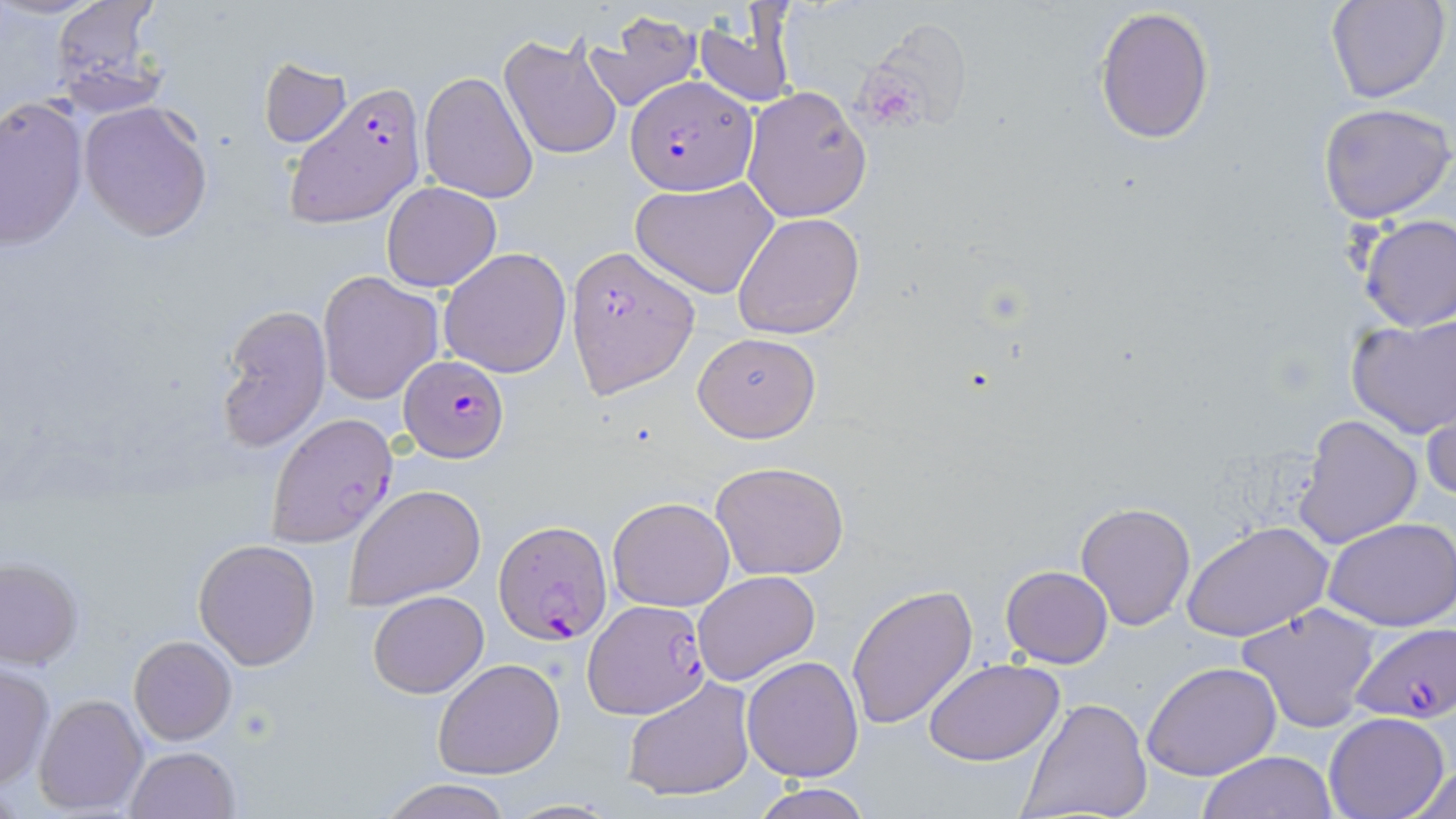
slide-level diagnosis = Plasmodium falciparum
field of view = one of a larger specimen
Plasmodium falciparum-infected red blood cell locations = approximate bounding boxes as (x1, y1, x2, y2) in pixels: (626, 75, 757, 197), (283, 82, 428, 224), (567, 244, 699, 398), (398, 355, 510, 462), (266, 412, 398, 546), (491, 520, 613, 645), (586, 600, 709, 719), (1350, 619, 1456, 726)
image size = 1456×819 pixels
preparation = thin blood film
uninfected red blood cell locations = approximate bounding boxes as (x1, y1, x2, y2) in pixels: (1328, 0, 1450, 103), (49, 1, 167, 108), (1094, 6, 1215, 144), (691, 10, 797, 111), (584, 11, 703, 113), (498, 30, 625, 162), (259, 56, 352, 149), (419, 72, 538, 203), (742, 84, 871, 222), (0, 99, 87, 251), (78, 100, 214, 241), (1317, 102, 1456, 223), (631, 177, 779, 298), (382, 182, 501, 293), (732, 212, 863, 340), (1356, 213, 1456, 332), (439, 247, 571, 378), (318, 271, 442, 403), (216, 304, 331, 450), (1347, 312, 1456, 438), (693, 331, 821, 442), (1421, 393, 1455, 509), (1294, 413, 1423, 549), (711, 461, 849, 580), (346, 484, 486, 611), (608, 497, 735, 612), (1076, 500, 1196, 630), (1325, 517, 1456, 630), (1183, 522, 1331, 642), (193, 537, 321, 669), (0, 556, 84, 669), (1001, 566, 1113, 668), (693, 570, 820, 684), (847, 584, 979, 730), (368, 589, 489, 697), (1237, 604, 1379, 730), (129, 635, 237, 745), (742, 657, 863, 782), (431, 658, 565, 779), (923, 658, 1064, 766), (1142, 662, 1283, 782), (0, 663, 54, 791), (620, 678, 755, 803), (33, 693, 149, 816), (1020, 698, 1151, 819), (1324, 712, 1450, 819), (124, 747, 240, 819), (1196, 750, 1338, 818), (1401, 763, 1456, 818), (380, 778, 512, 819), (748, 783, 873, 819), (499, 799, 622, 817)
modality = optical microscopy
magnification = 1000x
stain = May-Grünwald-Giemsa